Outline each uninfected red blood cell.
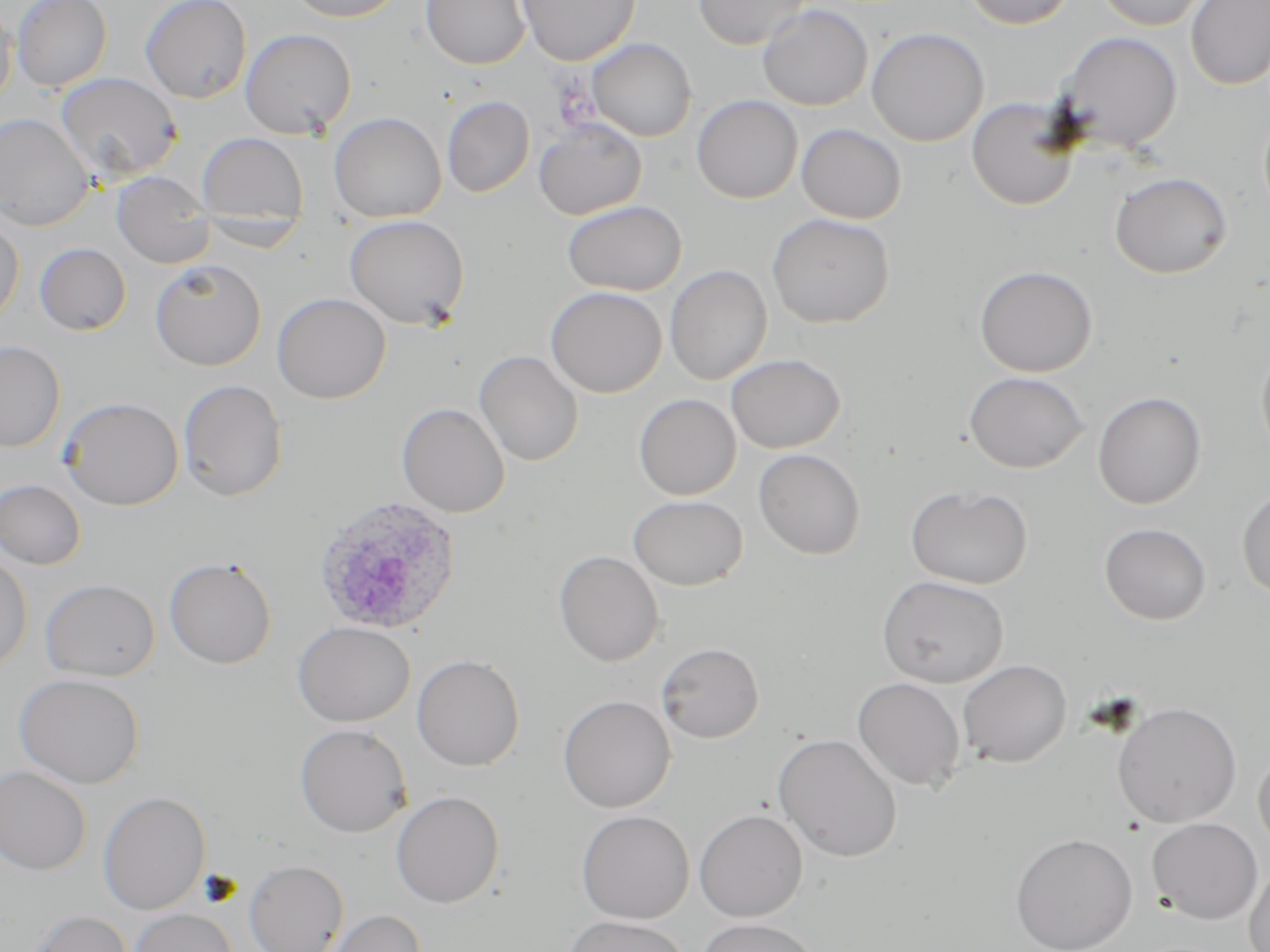

Approximate bounding boxes as named x1/y1/x2/y2 corners in pixels.
Uninfected red blood cells: (x1=12, y1=0, x2=112, y2=91), (x1=139, y1=0, x2=252, y2=104), (x1=283, y1=0, x2=407, y2=22), (x1=421, y1=0, x2=531, y2=69), (x1=516, y1=0, x2=640, y2=65), (x1=693, y1=0, x2=811, y2=50), (x1=961, y1=0, x2=1078, y2=30), (x1=1094, y1=0, x2=1212, y2=31), (x1=1185, y1=1, x2=1270, y2=90), (x1=0, y1=2, x2=16, y2=106), (x1=757, y1=3, x2=874, y2=111), (x1=866, y1=27, x2=989, y2=147), (x1=240, y1=28, x2=357, y2=139), (x1=1053, y1=31, x2=1184, y2=153), (x1=587, y1=38, x2=696, y2=142), (x1=55, y1=72, x2=182, y2=182), (x1=691, y1=95, x2=803, y2=204), (x1=442, y1=96, x2=535, y2=197), (x1=966, y1=96, x2=1081, y2=210), (x1=1258, y1=107, x2=1270, y2=221), (x1=329, y1=112, x2=446, y2=223), (x1=0, y1=113, x2=94, y2=230), (x1=533, y1=119, x2=647, y2=220), (x1=796, y1=124, x2=906, y2=224), (x1=196, y1=132, x2=309, y2=229), (x1=1110, y1=171, x2=1232, y2=278), (x1=112, y1=172, x2=214, y2=268), (x1=562, y1=199, x2=686, y2=296), (x1=766, y1=212, x2=895, y2=328), (x1=344, y1=214, x2=470, y2=330), (x1=0, y1=216, x2=24, y2=327), (x1=35, y1=242, x2=131, y2=336), (x1=150, y1=259, x2=267, y2=371), (x1=664, y1=264, x2=773, y2=385), (x1=974, y1=264, x2=1098, y2=377), (x1=545, y1=286, x2=667, y2=398), (x1=272, y1=292, x2=391, y2=404), (x1=0, y1=339, x2=66, y2=453), (x1=1255, y1=340, x2=1270, y2=462), (x1=474, y1=350, x2=583, y2=467), (x1=726, y1=354, x2=845, y2=453), (x1=963, y1=371, x2=1090, y2=473), (x1=177, y1=378, x2=288, y2=502), (x1=1092, y1=391, x2=1207, y2=509), (x1=633, y1=393, x2=741, y2=500), (x1=57, y1=396, x2=184, y2=510), (x1=396, y1=402, x2=510, y2=518), (x1=753, y1=448, x2=865, y2=559), (x1=0, y1=479, x2=87, y2=570), (x1=905, y1=483, x2=1033, y2=589), (x1=1236, y1=486, x2=1270, y2=599), (x1=628, y1=494, x2=748, y2=590), (x1=1099, y1=522, x2=1211, y2=625), (x1=0, y1=549, x2=32, y2=672), (x1=554, y1=550, x2=664, y2=666), (x1=164, y1=556, x2=277, y2=669), (x1=876, y1=575, x2=1008, y2=687), (x1=40, y1=578, x2=160, y2=682), (x1=293, y1=621, x2=415, y2=727), (x1=656, y1=642, x2=764, y2=743), (x1=412, y1=654, x2=525, y2=771), (x1=957, y1=659, x2=1071, y2=768), (x1=13, y1=673, x2=145, y2=788), (x1=852, y1=677, x2=966, y2=791), (x1=558, y1=694, x2=676, y2=812), (x1=1112, y1=701, x2=1241, y2=828), (x1=294, y1=723, x2=412, y2=837), (x1=773, y1=732, x2=903, y2=862), (x1=1253, y1=747, x2=1270, y2=854), (x1=0, y1=765, x2=91, y2=875), (x1=391, y1=790, x2=504, y2=908), (x1=98, y1=791, x2=211, y2=915), (x1=694, y1=809, x2=808, y2=922), (x1=576, y1=810, x2=695, y2=924), (x1=1146, y1=817, x2=1263, y2=924), (x1=1010, y1=832, x2=1138, y2=952), (x1=244, y1=859, x2=348, y2=952), (x1=1244, y1=862, x2=1270, y2=952), (x1=130, y1=908, x2=238, y2=952), (x1=27, y1=909, x2=133, y2=952), (x1=321, y1=909, x2=426, y2=952), (x1=563, y1=915, x2=690, y2=952), (x1=697, y1=918, x2=820, y2=952).

slide-level diagnosis = Plasmodium ovale
field of view = one of a larger specimen
Plasmodium ovale-infected red blood cell locations = approximate bounding boxes as named x1/y1/x2/y2 corners in pixels: (x1=311, y1=495, x2=462, y2=637)
stain = May-Grünwald-Giemsa
magnification = 1000x
preparation = thin blood film
modality = light microscopy
image size = 1270×952 pixels